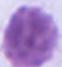
Summary:
  - Identification: red blood cell
  - Modality: micrograph
  - Magnification: 1000x